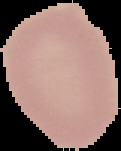

image size = 121×151 pixels
image type = segmented cell region on a black background
preparation = thin blood film
malaria status = uninfected